Comment on the morphology of the erythrocytes.
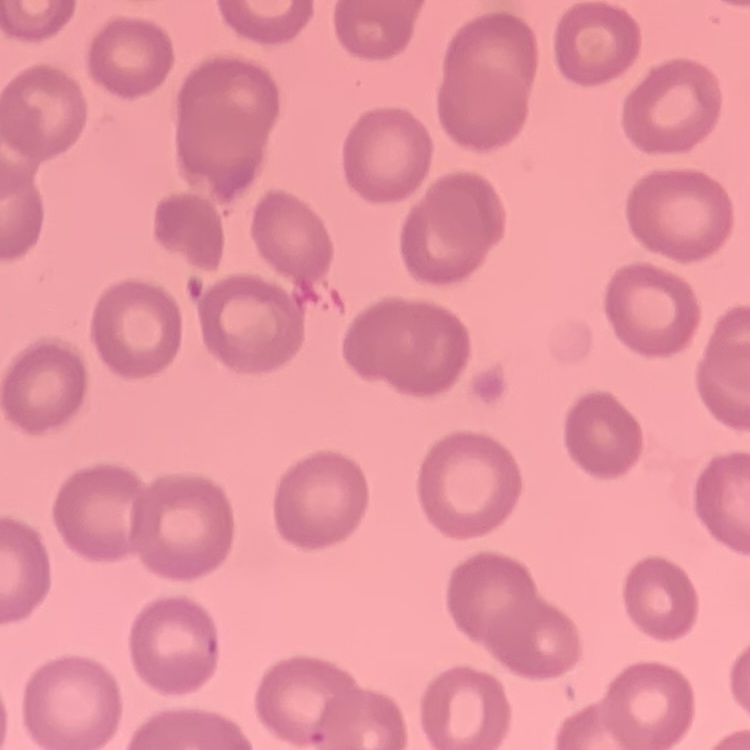
They show no rouleaux formation.

Stained with either Field's or Giemsa. Thin blood smear. One tile cut from a larger photomicrograph.